Comment on the morphology of the red blood cells.
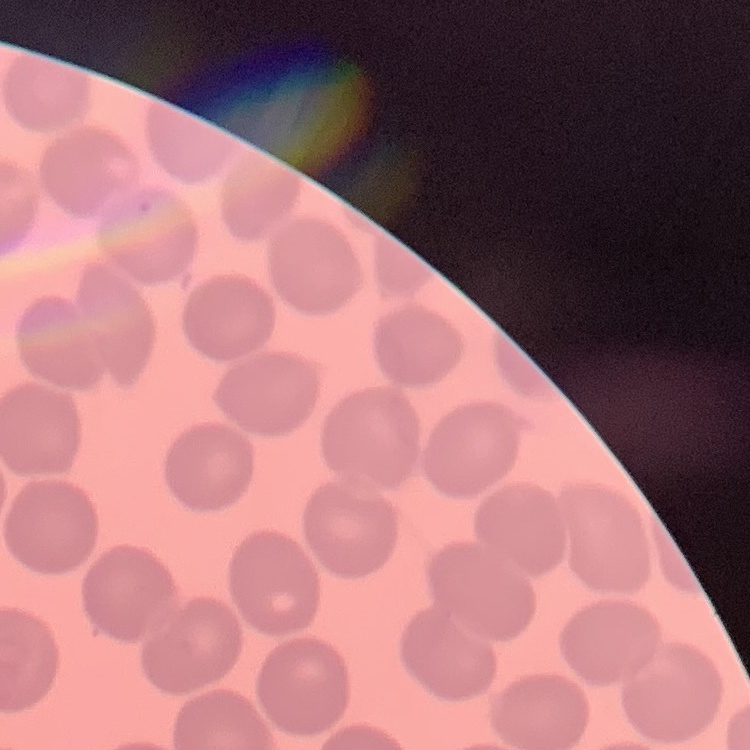
They show no rouleaux formation.

Summary:
  - Stain: Field's or Giemsa
  - Image type: one tile cut from a larger photomicrograph
  - Preparation: thin blood smear